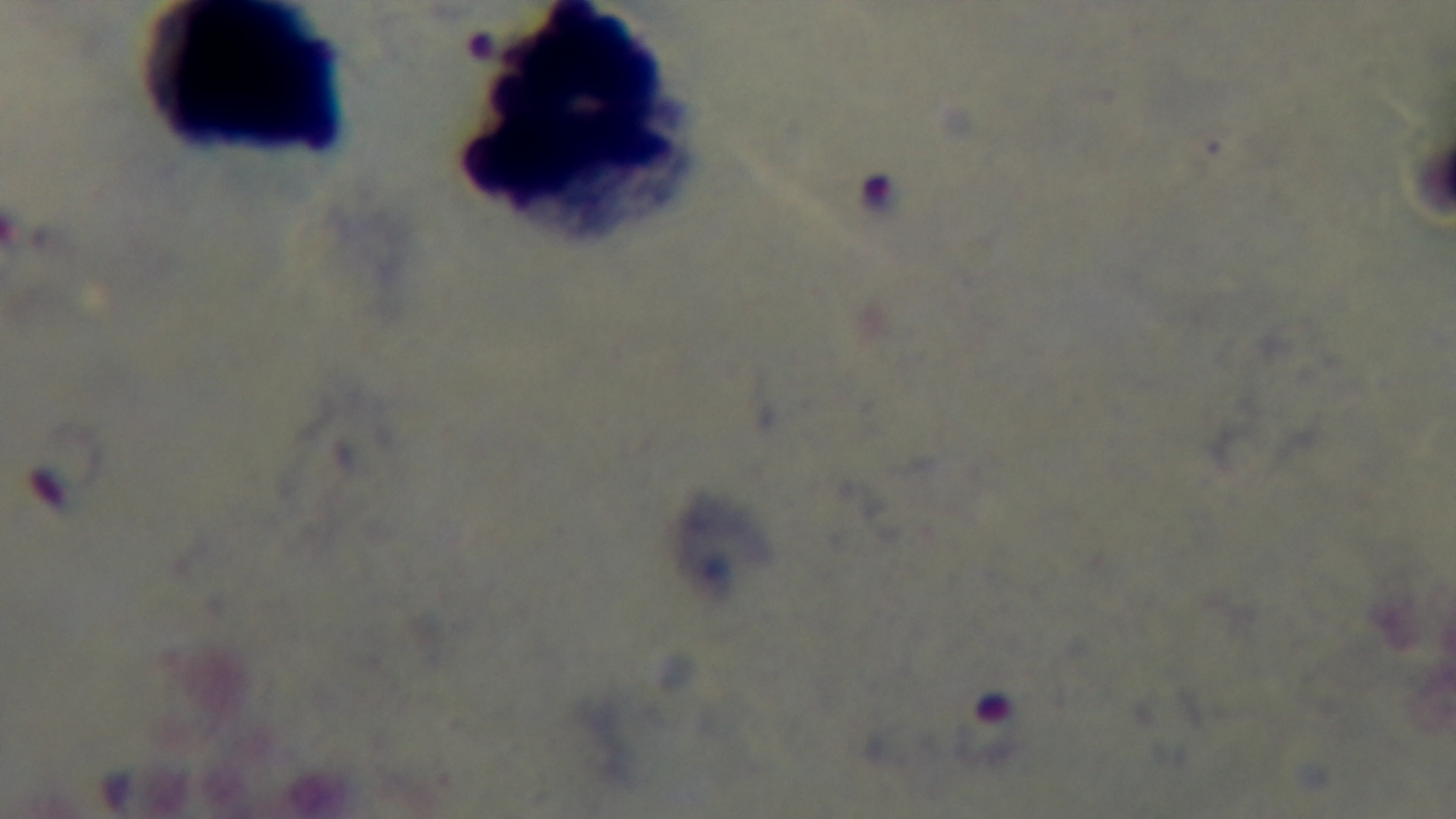

Malaria status: infected. Preparation: thick smear. Giemsa stain. 100x oil-immersion objective. Single field of view. Captured with a mounted 4K digital camera. Photomicrograph.